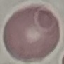

Summary:
  - Malaria status: uninfected
  - Stain: Giemsa
  - Image type: cell patch, automatically extracted from a larger field of view and resized to 64 × 64 pixels
  - Capture: smartphone camera at the microscope eyepiece
  - Preparation: thin smear